Assess this cell for malaria.
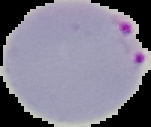

It is parasitized.

Summary:
  - Preparation: thin blood film
  - Image size: 151×127 pixels
  - Image type: cell region segmented out of the field of view; surrounding area masked to black